Report the malaria status of this cell.
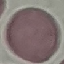

Uninfected.

capture = smartphone through the microscope eyepiece
stain = Giemsa
image type = automatically extracted cell patch, resized to 64 × 64 pixels
preparation = thin smear